Locate every blood parasite and identify its species.
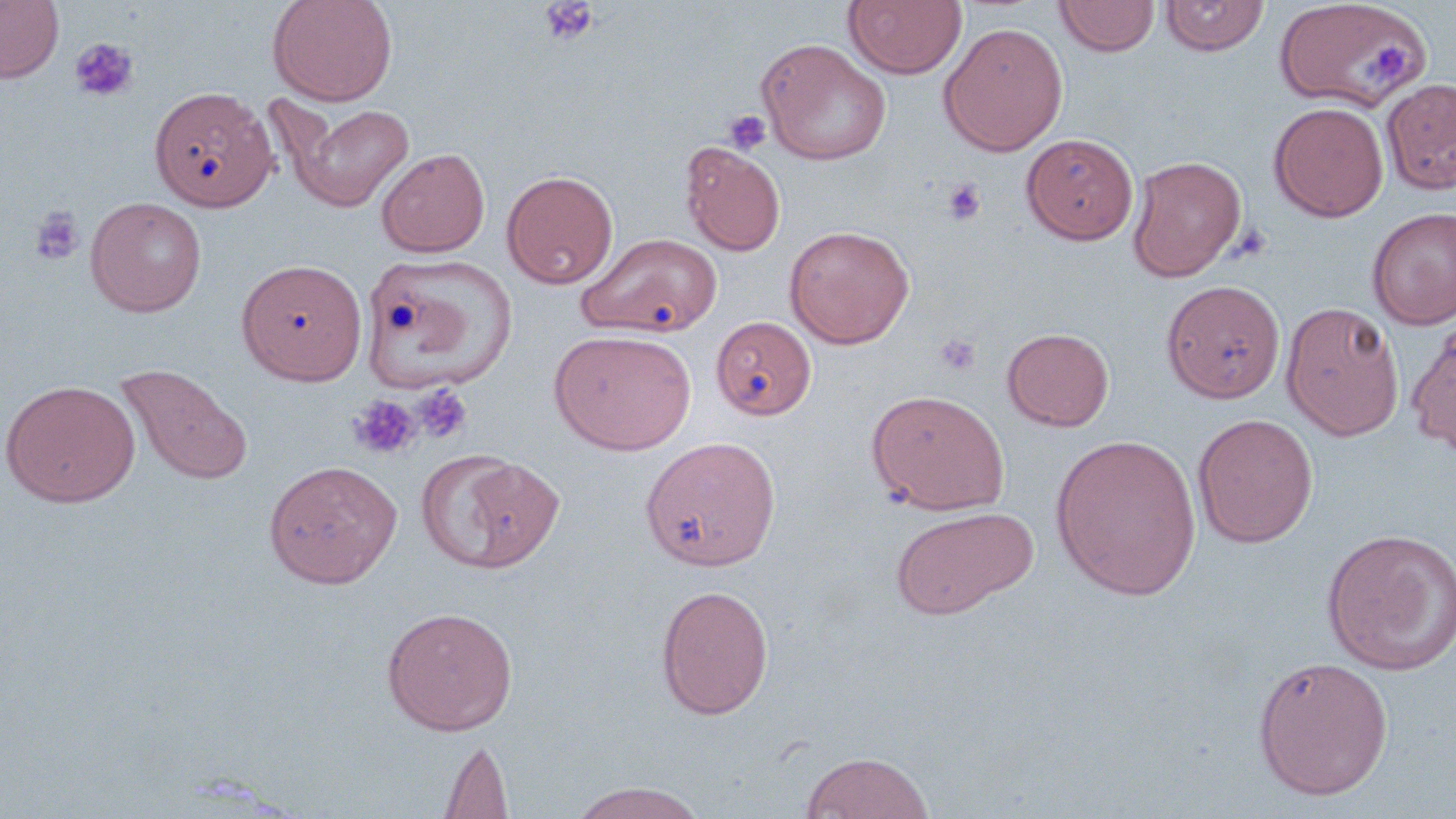
No blood parasites seen.

slide-level diagnosis = no evidence of blood parasites
preparation = thin blood film
uninfected red blood cell locations = approximate bounding boxes as (x1,y1)-(x2,y2) corner pairs in pixels: (0,0)-(63,84), (267,0)-(398,106), (843,0)-(966,80), (1054,0)-(1160,57), (1160,0)-(1270,56), (1273,1)-(1434,112), (938,22)-(1068,156), (756,38)-(892,166), (1380,76)-(1456,194), (149,85)-(277,212), (279,100)-(416,212), (1268,101)-(1388,222), (1021,133)-(1139,245), (681,141)-(786,256), (376,148)-(490,257), (1126,154)-(1247,282), (501,170)-(618,289), (85,196)-(207,317), (1367,207)-(1456,330), (784,224)-(915,349), (577,232)-(722,338), (359,253)-(518,394), (236,258)-(367,384), (1160,280)-(1285,403), (1280,301)-(1404,440), (711,316)-(816,421), (1406,322)-(1456,456), (1002,327)-(1114,431), (549,329)-(696,455), (116,364)-(254,487), (0,379)-(140,508), (866,389)-(1010,515), (1192,413)-(1318,548), (1050,434)-(1202,599), (640,436)-(780,571), (416,451)-(564,575), (263,459)-(402,588), (889,505)-(1039,620), (1319,528)-(1456,675), (655,584)-(774,720), (381,606)-(518,736), (1252,656)-(1394,800), (438,738)-(514,819), (800,751)-(934,818), (568,782)-(708,819)
modality = light microscopy
magnification = 1000x
platelet locations = approximate bounding boxes as (x1,y1)-(x2,y2) corner pairs in pixels: (539,0)-(599,47), (69,37)-(139,103), (1357,38)-(1413,91), (723,110)-(771,155), (942,178)-(987,225), (29,205)-(85,266), (936,334)-(981,376), (413,383)-(474,444), (348,395)-(420,460)
stain = May-Grünwald-Giemsa
field of view = one of a larger specimen
image size = 1456×819 pixels